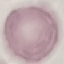

Summary:
  - Malaria status: uninfected
  - Stain: Giemsa
  - Capture: smartphone through the microscope eyepiece
  - Preparation: thin blood smear
  - Image type: automatically extracted cell patch, resized to 64 × 64 pixels